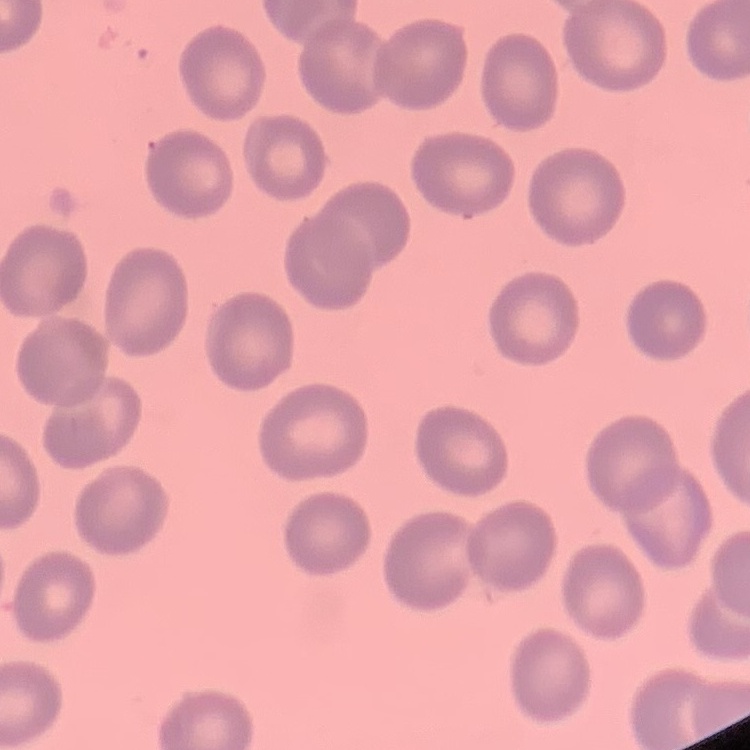

Summary:
  - Erythrocyte morphology: no rouleaux formation
  - Preparation: thin peripheral smear
  - Image type: square crop of a larger photomicrograph
  - Stain: Field's or Giemsa